Assess this cell for malaria.
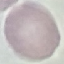

Uninfected.

Automatically extracted cell patch, resized to 64 × 64 pixels. Photographed with a smartphone camera at the microscope eyepiece. Giemsa-stained preparation. Thin smear of blood.